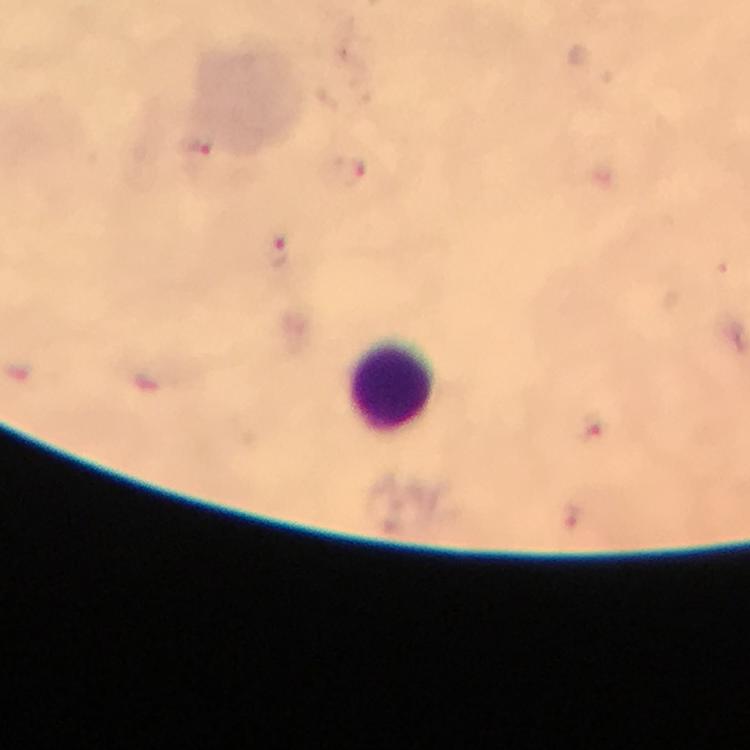 Approximate centers as (x, y) in pixels. Plasmodium parasite locations: (199, 145), (350, 171), (277, 249), (595, 428). Leukocyte locations: (394, 385). 100x magnification. Thick smear. Image is 750×750 pixels. Giemsa-stained preparation. Immersion oil applied. Cropped region of a single field of view. From a malaria diagnostic workup. Smartphone photograph taken through a microscope.